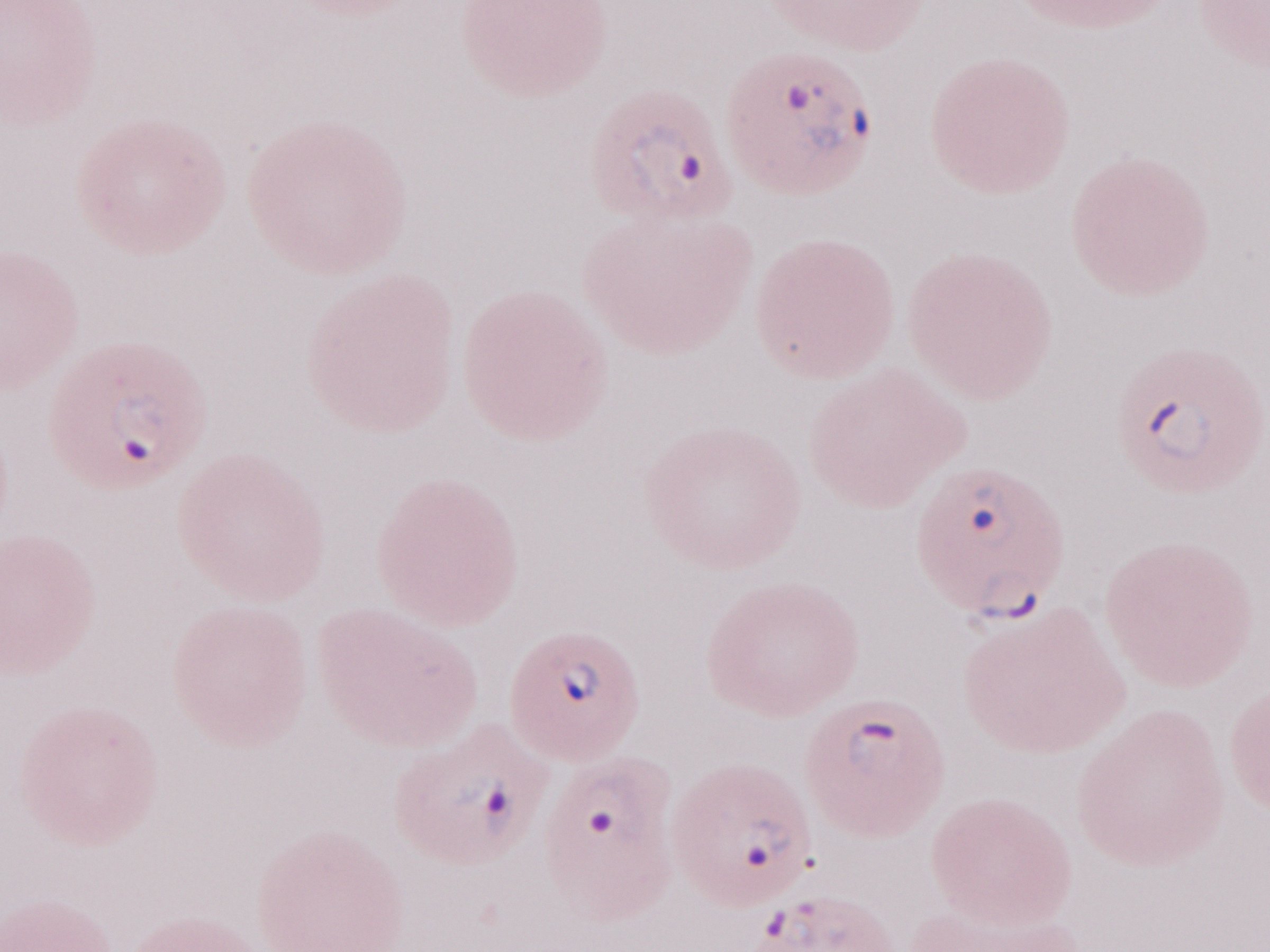

Malaria diagnosis (patient-level): positive. May-Grünwald-Giemsa-stained preparation. Single field of view. Magnification: 1,000x. Olympus BX43 microscope and DP73 digital camera. Image is 1270×952 pixels. Thin blood film.